Assess this cell for malaria.
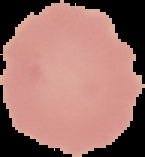

It is uninfected.

Summary:
  - Preparation: thin blood smear
  - Image size: 145×157 pixels
  - Image type: segmented cell region on a black background